Locate every leukocyte (white blood cell).
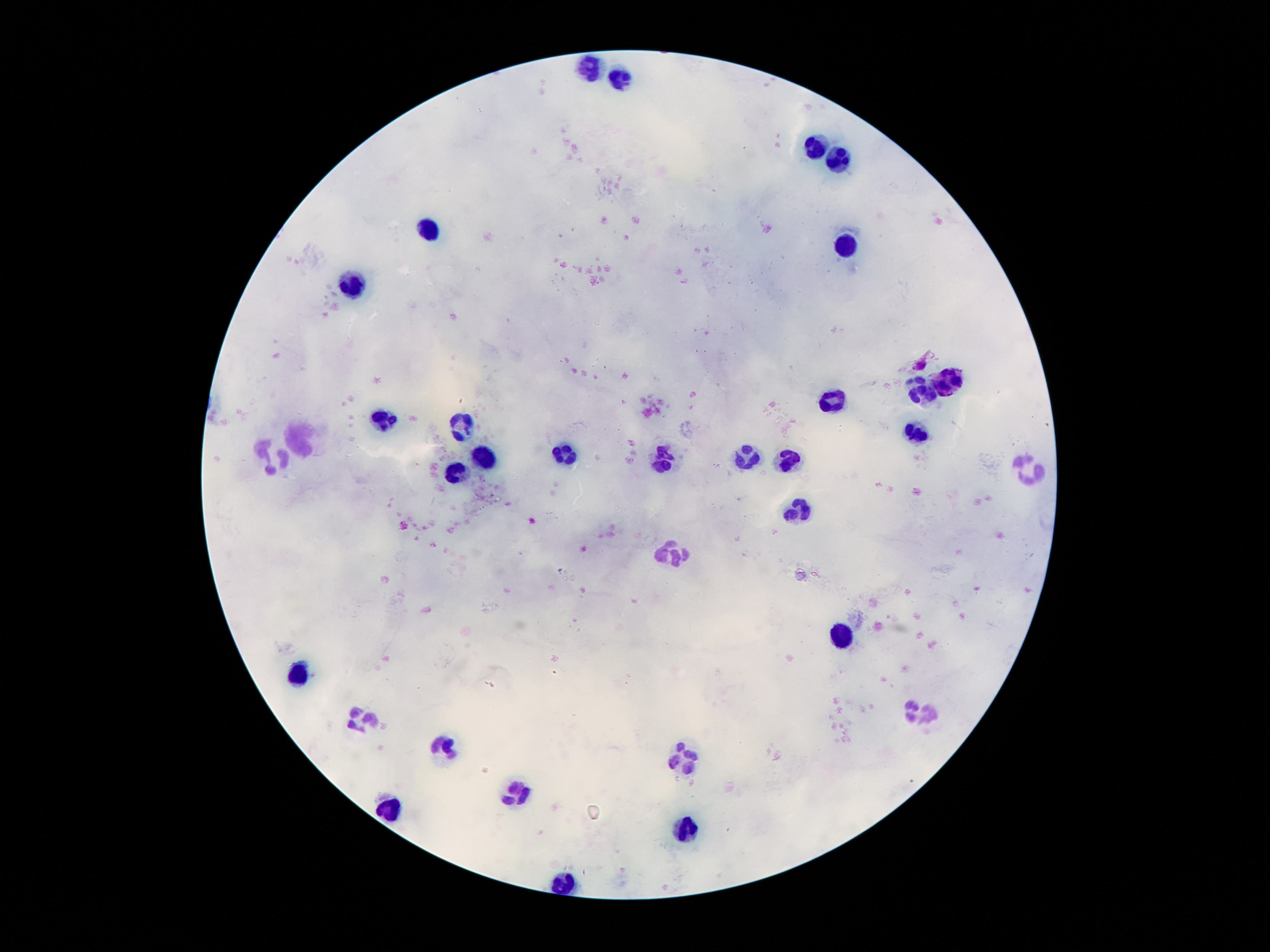
Approximate centers as {x, y} in pixels.
Leukocytes: {588, 64}, {619, 77}, {816, 147}, {836, 158}, {426, 229}, {846, 247}, {354, 285}, {948, 377}, {924, 389}, {835, 405}, {382, 420}, {460, 425}, {920, 430}, {298, 437}, {566, 455}, {743, 456}, {482, 458}, {661, 459}, {272, 460}, {787, 462}, {457, 473}, {1034, 473}, {796, 510}, {672, 552}, {840, 638}, {300, 672}, {922, 712}, {363, 720}, {446, 748}, {683, 759}, {511, 788}, {387, 813}, {687, 829}.

{
  "preparation": "thick blood smear",
  "field_of_view": "single",
  "capture": "smartphone camera through the microscope eyepiece",
  "stain": "Giemsa",
  "patient_malaria_status": "not infected",
  "image_size": "1270×952 pixels",
  "magnification": "100x"
}